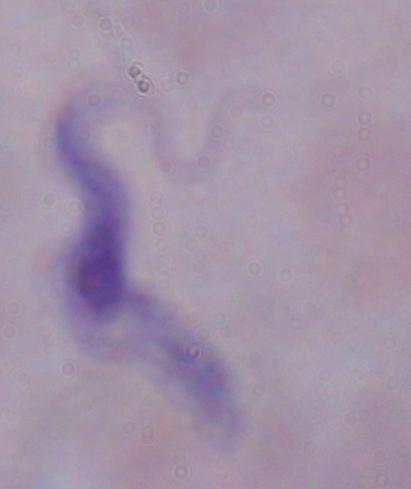 A trypanosome is seen. Micrograph. 1000x magnification.